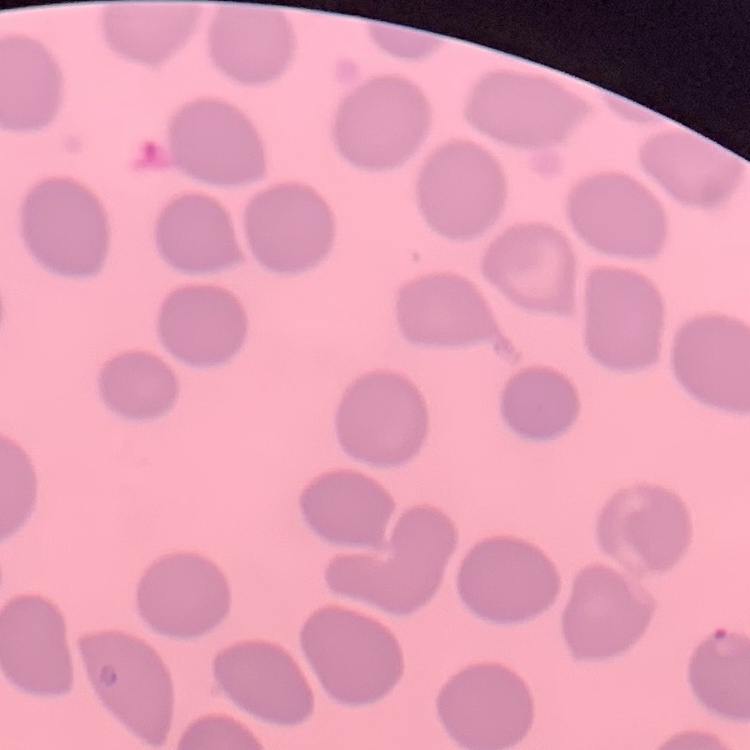

red_blood_cell_morphology: no rouleaux formation
stain: Field's or Giemsa
image_type: square crop of a larger photomicrograph
preparation: thin peripheral smear